Outline each blood parasite and name the species.
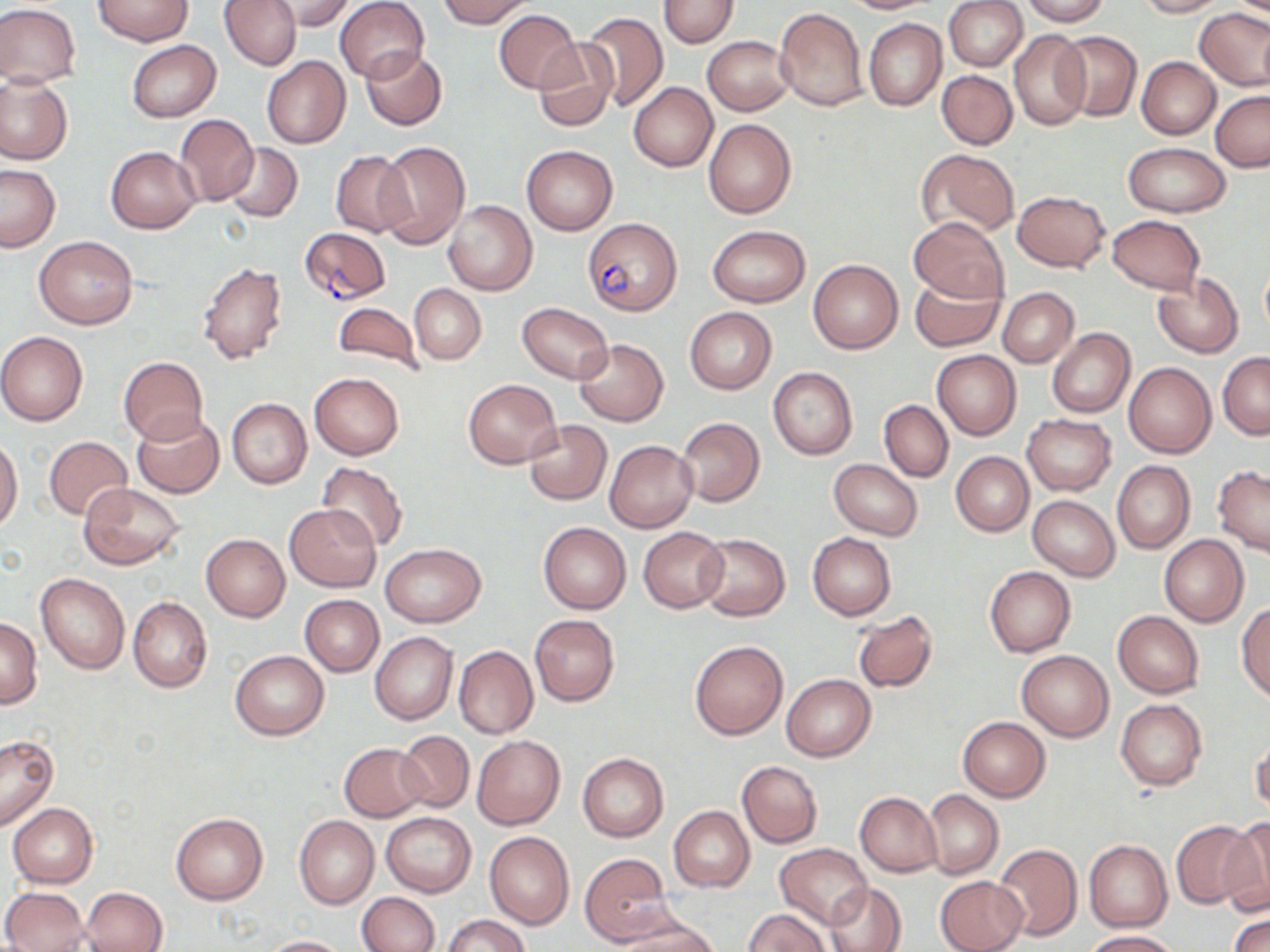

Approximate bounding boxes as (x1, y1, x2, y2) in pixels.
Plasmodium falciparum-infected red blood cells: (582, 216, 682, 315), (299, 228, 390, 306).
No Plasmodium ovale, Plasmodium malariae, Plasmodium vivax, Babesia divergens, or Trypanosoma brucei observed.

{
  "slide_level_diagnosis": "Plasmodium falciparum",
  "preparation": "thin blood film",
  "image_size": "1270×952 pixels",
  "magnification": "1000x",
  "field_of_view": "single",
  "stain": "May-Grünwald-Giemsa",
  "uninfected_red_blood_cell_locations": "approximate bounding boxes as (x1, y1, x2, y2) in pixels: (93, 0, 191, 46), (219, 0, 300, 70), (336, 0, 429, 84), (437, 0, 535, 27), (658, 0, 738, 47), (837, 0, 936, 13), (945, 0, 1027, 71), (1021, 0, 1109, 26), (1134, 0, 1226, 17), (265, 1, 357, 31), (0, 4, 80, 87), (773, 7, 868, 112), (1194, 8, 1270, 91), (494, 9, 580, 93), (578, 11, 668, 111), (863, 18, 946, 110), (1009, 30, 1092, 131), (1055, 31, 1141, 120), (703, 36, 793, 115), (127, 39, 221, 121), (532, 39, 620, 132), (360, 47, 447, 130), (262, 56, 350, 148), (1136, 57, 1219, 139), (937, 70, 1018, 150), (0, 76, 72, 165), (628, 83, 717, 172), (1210, 90, 1270, 171), (174, 115, 259, 206), (704, 118, 797, 219), (375, 141, 470, 248), (222, 143, 302, 222), (1123, 143, 1231, 217), (520, 144, 617, 234), (105, 145, 202, 233), (917, 148, 1019, 237), (330, 150, 413, 239), (0, 164, 60, 251), (1013, 191, 1109, 272), (442, 200, 537, 296), (909, 215, 1009, 305), (1107, 215, 1205, 293), (709, 225, 809, 307), (35, 235, 137, 329), (808, 259, 903, 353), (198, 261, 288, 364), (1260, 265, 1270, 336), (1152, 273, 1244, 357), (910, 276, 1003, 351), (410, 283, 487, 364), (997, 288, 1079, 367), (330, 299, 425, 375), (517, 303, 613, 383), (684, 307, 776, 393), (1047, 327, 1135, 418), (0, 332, 88, 425), (573, 339, 668, 425), (931, 349, 1022, 440), (1219, 351, 1270, 438), (118, 356, 208, 444), (1123, 361, 1216, 458), (768, 367, 857, 459), (310, 372, 404, 459), (464, 378, 561, 468), (227, 399, 312, 488), (878, 400, 952, 482), (131, 414, 223, 498), (1022, 414, 1115, 495), (676, 417, 764, 507), (524, 420, 611, 505), (0, 436, 23, 535), (43, 436, 133, 521), (605, 440, 697, 533), (951, 451, 1033, 536), (828, 459, 923, 540), (1112, 461, 1194, 553), (317, 462, 407, 549), (1213, 466, 1270, 557), (79, 484, 186, 569), (1027, 496, 1119, 580), (286, 503, 380, 591), (538, 522, 630, 613), (638, 527, 728, 612), (695, 532, 790, 620), (808, 533, 896, 619), (201, 534, 290, 620), (1159, 535, 1248, 627), (381, 544, 485, 627), (984, 566, 1075, 657), (36, 572, 130, 674), (299, 595, 383, 677), (128, 596, 212, 693), (1236, 602, 1270, 703), (852, 609, 938, 693), (1113, 611, 1204, 698), (529, 615, 620, 707), (0, 617, 43, 708), (370, 632, 457, 724), (688, 639, 788, 740), (454, 646, 538, 739), (229, 650, 329, 740), (1016, 650, 1114, 741), (781, 674, 875, 761), (1116, 699, 1207, 790), (957, 716, 1050, 801), (396, 730, 474, 813), (471, 734, 565, 829), (1250, 734, 1270, 817), (0, 736, 59, 831), (339, 743, 428, 821), (578, 753, 668, 841), (737, 760, 822, 848), (922, 789, 1003, 879), (855, 791, 942, 876), (8, 803, 97, 888), (669, 806, 753, 891), (381, 812, 476, 896), (171, 813, 267, 904), (294, 815, 379, 908), (1219, 819, 1270, 914), (1172, 820, 1255, 907), (485, 831, 574, 929), (1085, 840, 1172, 931), (775, 843, 871, 928), (993, 844, 1082, 942), (580, 852, 673, 947), (933, 875, 1028, 952), (825, 881, 907, 952), (81, 886, 168, 952), (3, 887, 89, 952), (359, 891, 439, 952), (744, 908, 829, 951), (1229, 910, 1270, 952), (616, 913, 720, 951), (443, 914, 528, 952), (1084, 930, 1182, 951), (259, 936, 352, 952)",
  "modality": "optical microscopy"
}